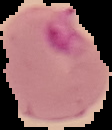

Image is 112×130 pixels. From a thin blood smear. Segmented cell region on a black background. Malaria status: parasitized.